Outline each Plasmodium ovale-infected red blood cell.
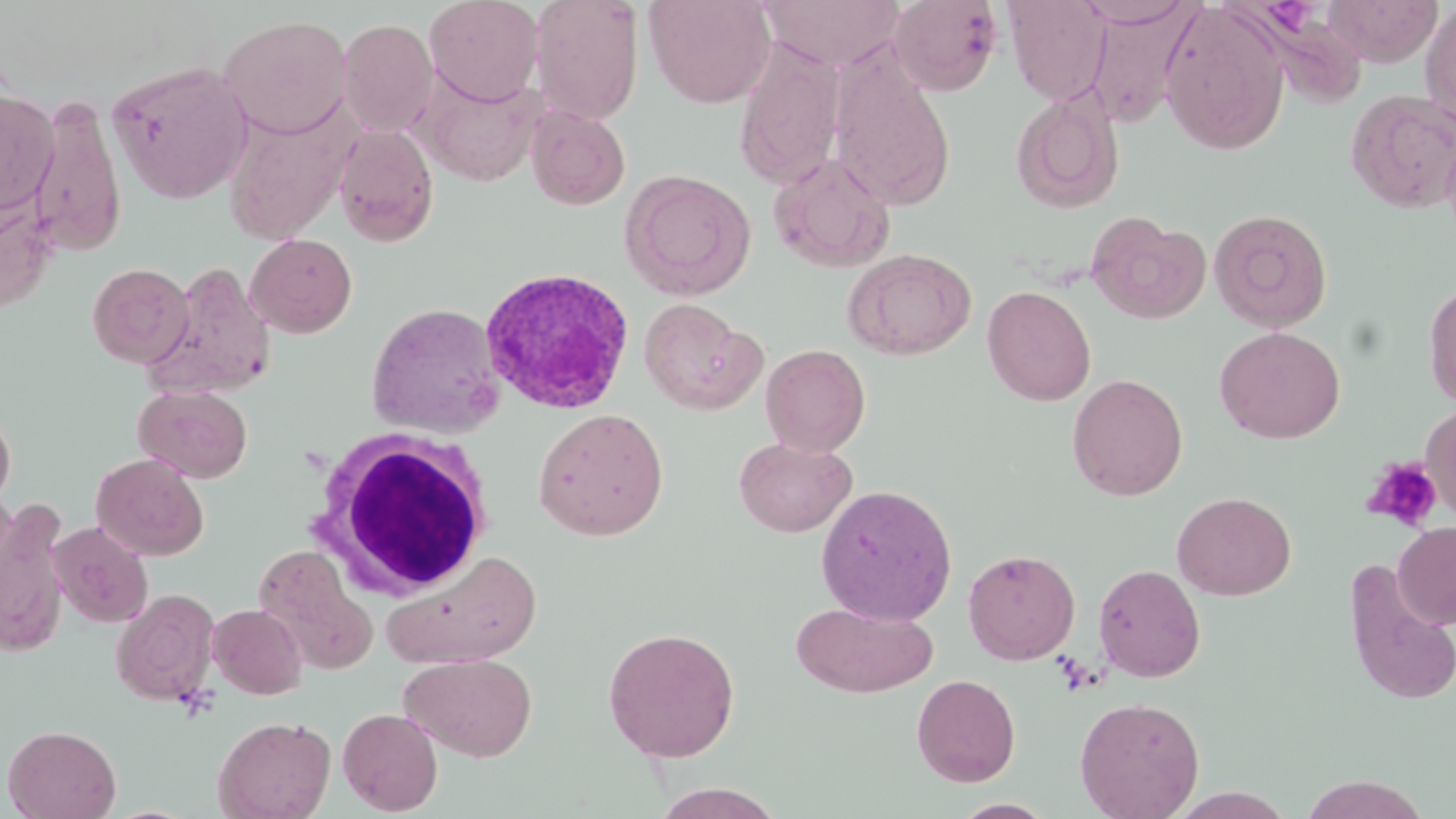

Approximate bounding boxes as (x1,y1)-(x2,y2) corner pairs in pixels.
Plasmodium ovale-infected red blood cells: (478,266)-(634,415).

slide-level diagnosis = Plasmodium ovale
field of view = one of a larger specimen
stain = May-Grünwald-Giemsa
white blood cell locations = approximate bounding boxes as (x1,y1)-(x2,y2) corner pairs in pixels: (313,428)-(495,598)
uninfected red blood cell locations = approximate bounding boxes as (x1,y1)-(x2,y2) corner pairs in pixels: (423,0)-(544,105), (530,0)-(644,124), (644,0)-(775,108), (758,0)-(904,69), (891,0)-(1002,95), (1004,0)-(1110,104), (1322,0)-(1442,67), (1074,1)-(1195,29), (1160,3)-(1290,155), (1421,3)-(1456,132), (1085,7)-(1197,129), (219,13)-(351,140), (337,18)-(438,136), (733,36)-(846,190), (828,41)-(957,212), (107,59)-(253,203), (419,73)-(544,186), (0,88)-(60,215), (1010,89)-(1124,213), (1346,89)-(1456,212), (29,95)-(127,258), (526,105)-(630,210), (333,124)-(439,247), (1441,125)-(1456,249), (768,152)-(896,272), (620,169)-(757,300), (1208,208)-(1333,332), (1086,211)-(1210,324), (245,233)-(357,338), (843,248)-(977,360), (145,261)-(277,400), (87,262)-(193,367), (1423,279)-(1456,409), (983,285)-(1096,406), (640,298)-(762,415), (365,302)-(506,438), (1214,326)-(1345,444), (761,344)-(871,457), (1067,373)-(1188,501), (134,384)-(253,483), (1420,401)-(1456,524), (532,407)-(669,540), (0,409)-(16,511), (733,437)-(857,537), (92,453)-(209,561), (816,483)-(957,625), (0,486)-(17,581), (1172,491)-(1296,600), (0,500)-(71,657), (49,521)-(153,628), (1392,522)-(1456,629), (253,545)-(378,674), (383,548)-(543,669), (963,548)-(1080,664), (1342,560)-(1456,706), (1093,563)-(1206,682), (111,587)-(221,707), (789,600)-(940,698), (208,604)-(307,699), (602,626)-(740,762), (400,652)-(538,762), (911,673)-(1021,787), (1074,696)-(1205,818), (337,707)-(443,815), (213,715)-(336,819), (2,724)-(121,819), (1297,774)-(1433,819), (650,782)-(786,818), (1169,788)-(1296,818), (949,798)-(1059,818)
platelet locations = approximate bounding boxes as (x1,y1)-(x2,y2) corner pairs in pixels: (1362,456)-(1443,531)
magnification = 1000x
preparation = thin blood film
modality = optical microscopy
image size = 1456×819 pixels